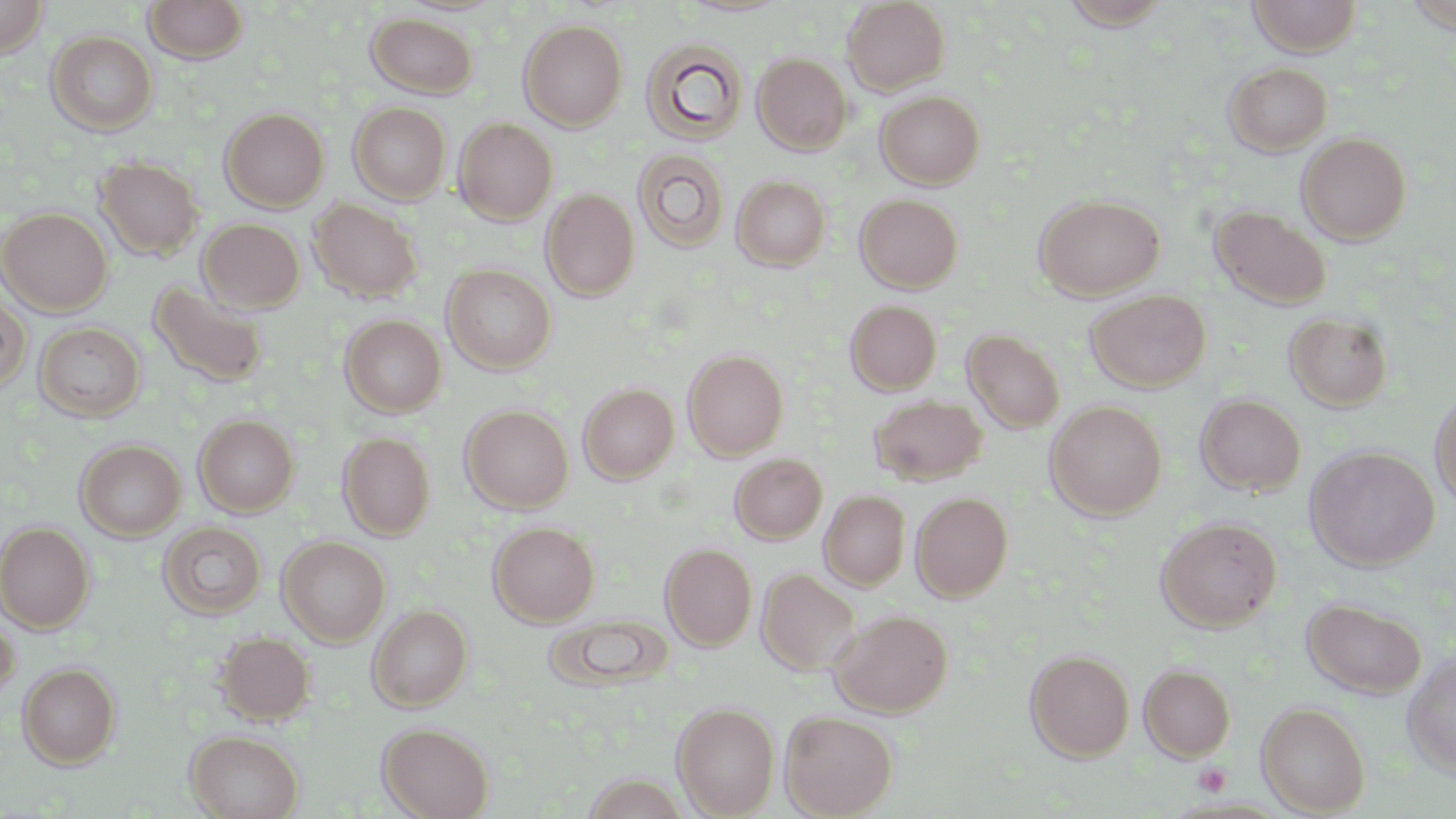
Summary:
  - Coordinate format: approximate bounding boxes as (x1,y1)-(x2,y2) corner pairs in pixels
  - Platelet locations: (1194,763)-(1231,796)
  - Uninfected red blood cell locations: (0,0)-(50,58), (143,0)-(249,64), (1246,0)-(1363,56), (842,1)-(951,95), (1058,1)-(1173,30), (1403,3)-(1456,36), (366,12)-(479,98), (518,19)-(628,130), (46,30)-(158,136), (640,37)-(749,146), (752,53)-(852,154), (1224,61)-(1332,155), (876,90)-(985,189), (349,102)-(451,204), (220,107)-(330,212), (454,117)-(558,224), (1296,132)-(1412,245), (632,149)-(729,252), (94,156)-(203,260), (731,175)-(831,270), (541,189)-(640,301), (855,193)-(963,293), (1034,195)-(1165,299), (308,198)-(423,303), (1211,206)-(1331,310), (0,207)-(113,315), (197,218)-(305,312), (442,264)-(556,374), (148,281)-(269,388), (1085,289)-(1211,392), (0,293)-(30,395), (844,299)-(942,395), (1284,311)-(1392,412), (339,314)-(447,417), (33,321)-(146,422), (963,329)-(1066,433), (682,349)-(789,460), (578,383)-(679,483), (1429,388)-(1456,510), (1195,393)-(1306,496), (869,395)-(987,485), (1045,401)-(1167,519), (460,404)-(574,513), (194,414)-(299,517), (338,431)-(435,540), (75,439)-(186,541), (1305,446)-(1440,571), (730,453)-(828,544), (819,490)-(910,590), (911,492)-(1013,601), (1156,516)-(1282,632), (0,521)-(95,632), (488,521)-(599,626), (159,522)-(267,620), (277,536)-(390,646), (660,543)-(757,650), (757,567)-(861,677), (1302,598)-(1426,699), (368,605)-(473,711), (0,609)-(20,708), (830,609)-(953,717), (547,614)-(671,692), (215,631)-(315,725), (1025,649)-(1135,761), (1402,653)-(1456,778), (17,663)-(121,769), (1139,663)-(1235,760), (1257,701)-(1370,816), (672,702)-(779,817), (779,710)-(899,818), (378,722)-(494,819), (186,730)-(304,818)
  - Slide-level diagnosis: no evidence of blood parasites
  - Magnification: 1000x
  - Field of view: one of a larger specimen
  - Image size: 1456×819 pixels
  - Preparation: thin blood smear
  - Modality: optical microscopy
  - Stain: May-Grünwald-Giemsa